Locate every Plasmodium parasite.
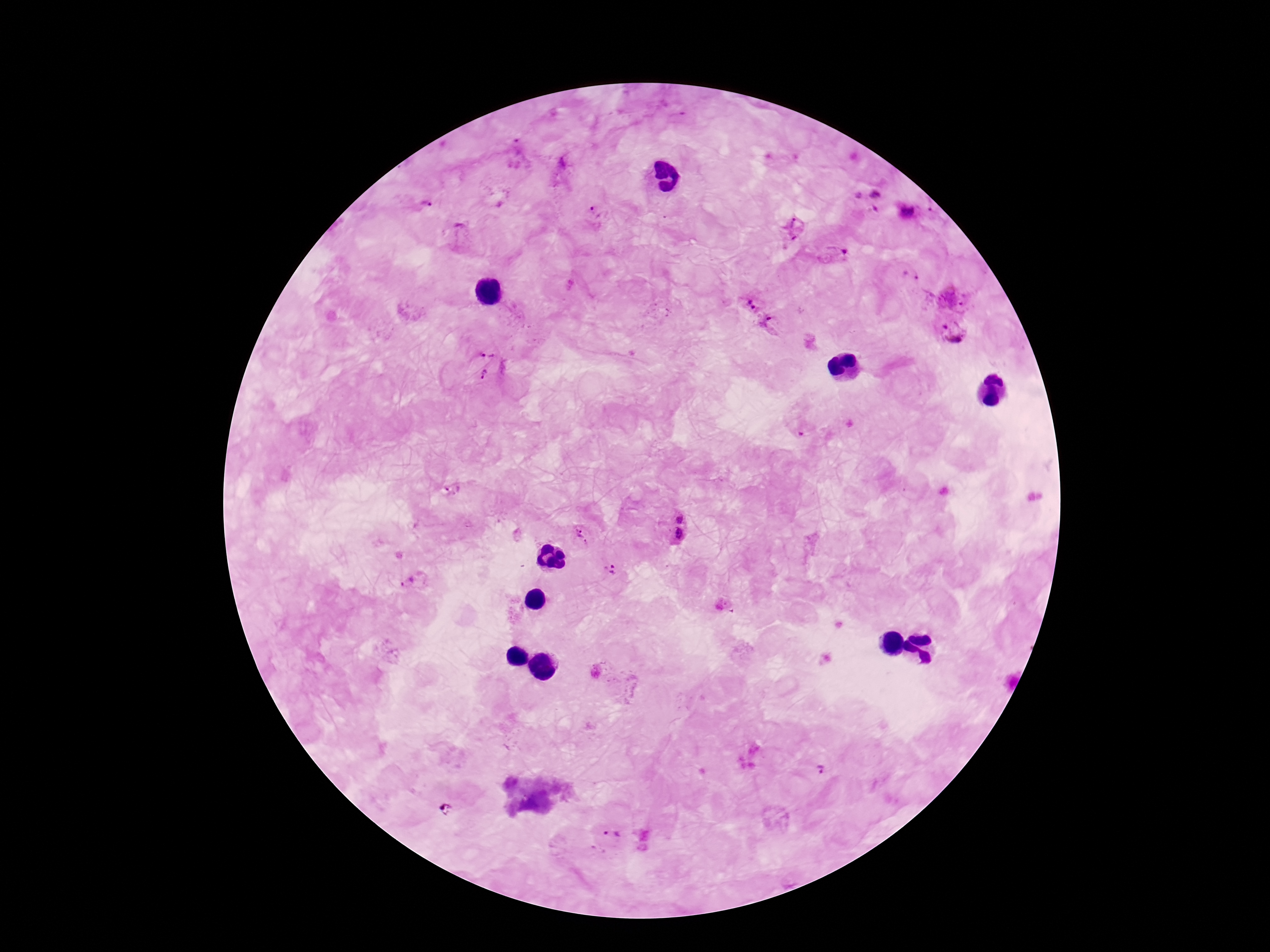

Approximate object centers, in pixels from the top-left corner.
Plasmodium parasites: (x=515, y=154), (x=561, y=167), (x=868, y=200), (x=420, y=204), (x=908, y=210), (x=593, y=215), (x=794, y=227), (x=460, y=232), (x=838, y=254), (x=911, y=277), (x=955, y=296), (x=748, y=299), (x=772, y=326), (x=953, y=330), (x=489, y=349), (x=483, y=372), (x=805, y=432), (x=451, y=490), (x=680, y=514), (x=578, y=529), (x=674, y=535), (x=587, y=543), (x=611, y=568), (x=415, y=582), (x=821, y=769), (x=613, y=836).

Summary:
  - Capture: smartphone camera through the microscope eyepiece
  - Field of view: one from this slide
  - Preparation: thick blood smear
  - Patient malaria status: positive
  - Stain: Giemsa
  - Magnification: 100x
  - Image size: 1270×952 pixels